Describe the morphology of the red blood cells.
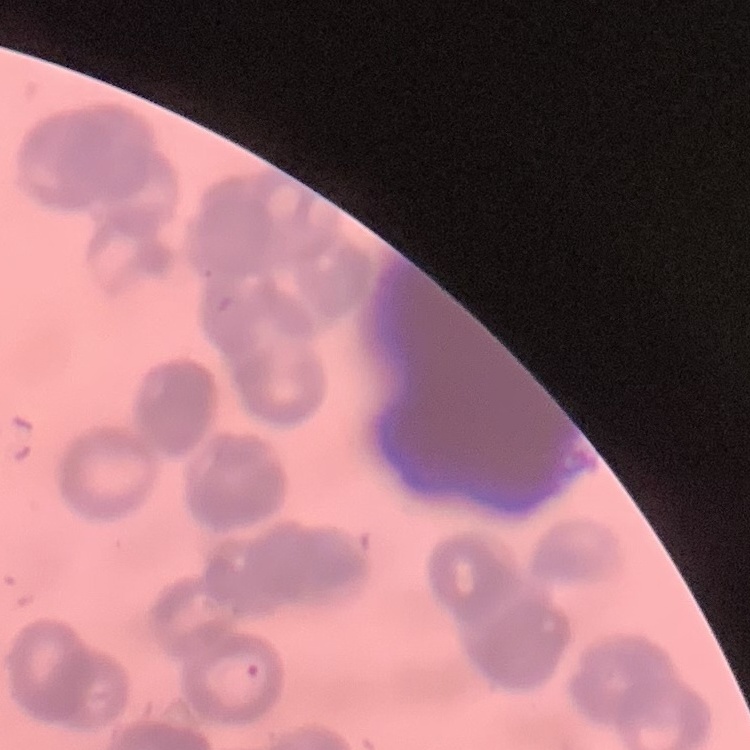

They show rouleaux formation.

Stained with either Field's or Giemsa. Thin peripheral smear. One tile cut from a larger photomicrograph.